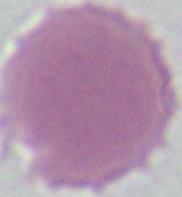

{
  "magnification": "1000x",
  "modality": "photomicrograph",
  "identification": "red blood cell"
}